Report the malaria status of this cell.
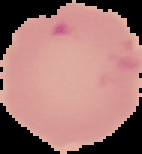
Parasitized.

Image is 142×154 pixels. Segmented cell region on a black background. From a thin blood film.